Report the malaria status of this cell.
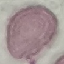
Uninfected.

Thin blood film. Acquired by smartphone through the microscope eyepiece. Cell patch, automatically extracted from a larger field of view and resized to 64 × 64 pixels. Giemsa-stained preparation.